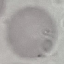
Summary:
  - Result: no malaria parasites detected
  - Capture: smartphone through the microscope eyepiece
  - Stain: Giemsa
  - Preparation: thin blood film
  - Image type: automatically extracted cell patch, resized to 64 × 64 pixels